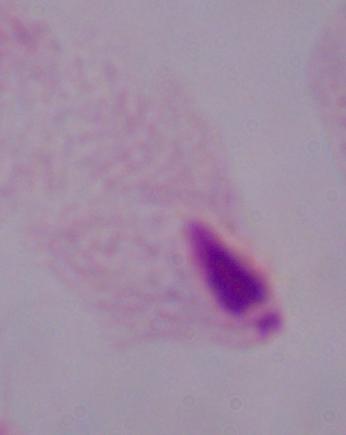
A trichomonad is shown. Micrograph. 1000x magnification.